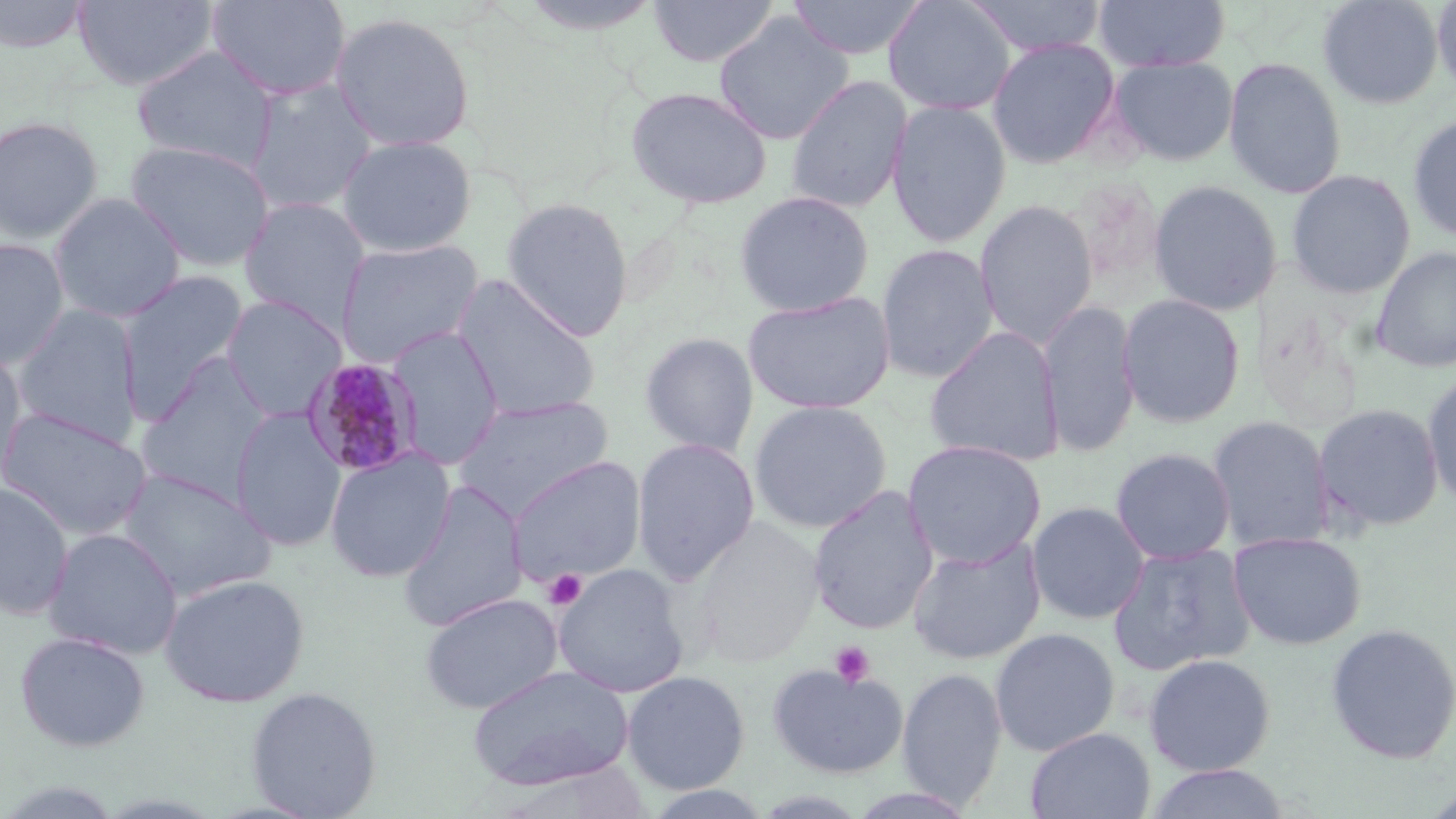

{
  "slide_level_diagnosis": "Plasmodium malariae",
  "field_of_view": "one of a larger specimen",
  "modality": "optical microscopy",
  "plasmodium_malariae_infected_red_blood_cell_locations": "approximate bounding boxes as (x1,y1)-(x2,y2) corner pairs in pixels: (300,357)-(425,477)",
  "magnification": "1000x",
  "platelet_locations": "approximate bounding boxes as (x1,y1)-(x2,y2) corner pairs in pixels: (543,569)-(587,610), (830,641)-(875,688)",
  "uninfected_red_blood_cell_locations": "approximate bounding boxes as (x1,y1)-(x2,y2) corner pairs in pixels: (0,0)-(92,53), (73,0)-(218,91), (205,0)-(352,101), (221,0)-(360,202), (648,0)-(779,67), (785,0)-(928,60), (882,0)-(1016,116), (964,0)-(1108,58), (1092,0)-(1231,72), (1317,0)-(1444,109), (1431,0)-(1456,98), (329,11)-(476,153), (714,12)-(854,145), (987,37)-(1122,169), (130,44)-(279,173), (1107,56)-(1238,166), (1223,57)-(1347,199), (786,75)-(912,214), (245,79)-(380,213), (625,85)-(773,209), (886,99)-(1012,249), (1406,113)-(1456,241), (0,115)-(105,244), (336,134)-(477,257), (125,139)-(275,272), (1285,169)-(1416,299), (1148,179)-(1282,316), (733,189)-(875,317), (49,193)-(186,323), (500,196)-(635,340), (238,197)-(372,330), (974,200)-(1098,348), (0,237)-(70,370), (336,239)-(483,366), (875,243)-(999,383), (1370,246)-(1456,372), (116,269)-(251,420), (452,276)-(602,421), (742,290)-(895,414), (1118,293)-(1246,428), (220,295)-(347,421), (1039,300)-(1140,458), (11,303)-(144,447), (387,326)-(505,470), (924,326)-(1065,467), (639,331)-(759,457), (0,344)-(30,493), (134,358)-(275,504), (1422,368)-(1456,512), (452,396)-(615,518), (748,400)-(892,534), (1312,402)-(1445,533), (0,406)-(153,541), (230,407)-(346,553), (1206,415)-(1335,552), (631,437)-(760,585), (903,439)-(1047,567), (1110,446)-(1236,564), (325,449)-(455,582), (506,455)-(647,588), (116,467)-(277,601), (396,479)-(529,633), (0,481)-(74,621), (806,484)-(940,635), (1027,501)-(1150,625), (691,518)-(826,667), (42,527)-(184,660), (1228,530)-(1367,650), (908,537)-(1046,665), (1108,543)-(1256,676), (551,563)-(690,699), (159,573)-(310,707), (420,593)-(563,715), (1325,623)-(1456,764), (990,627)-(1120,756), (15,631)-(150,752), (1143,653)-(1276,776), (767,663)-(909,778), (467,664)-(634,791), (896,666)-(1007,810), (621,670)-(751,795), (245,685)-(382,818), (1025,727)-(1155,819), (1142,763)-(1293,819), (640,785)-(778,818)",
  "preparation": "thin blood film",
  "stain": "May-Grünwald-Giemsa",
  "image_size": "1456×819 pixels"
}